Assess this cell for malaria.
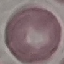

It is uninfected.

Automatically extracted cell patch, resized to 64 × 64 pixels. Photographed with a smartphone camera at the microscope eyepiece. Thin smear of blood. Giemsa stain.